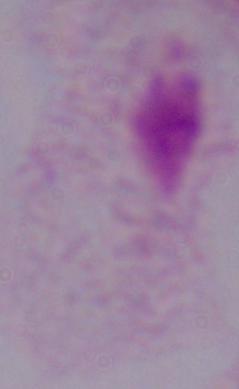
modality = micrograph
identification = trichomonad
magnification = 1000x